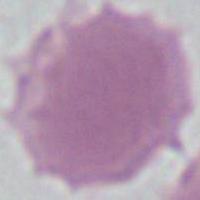

An erythrocyte is seen. 1000x magnification. Photomicrograph.